Comment on the morphology of the erythrocytes.
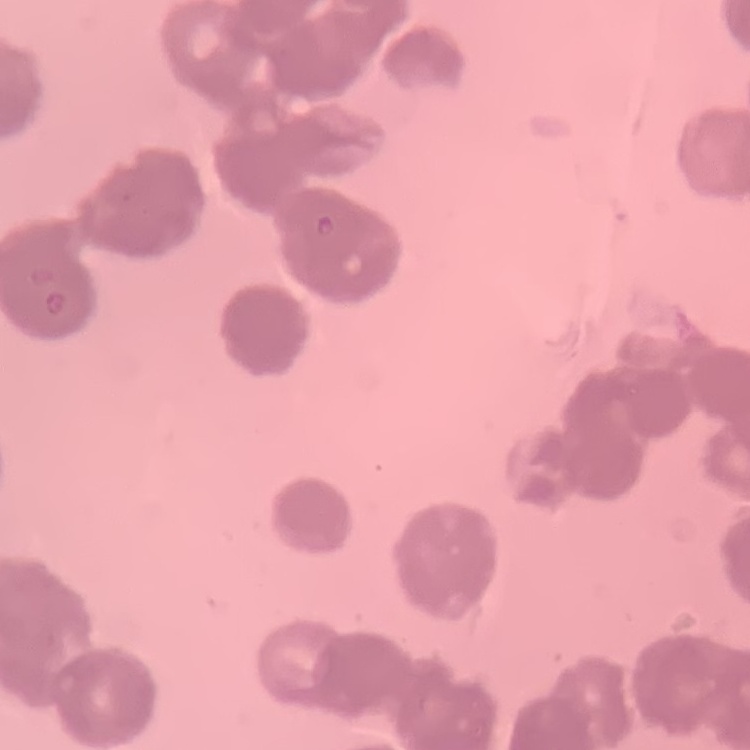

Rouleaux formation.

Summary:
  - Stain: Field's or Giemsa
  - Image type: square crop of a larger photomicrograph
  - Preparation: thin peripheral smear